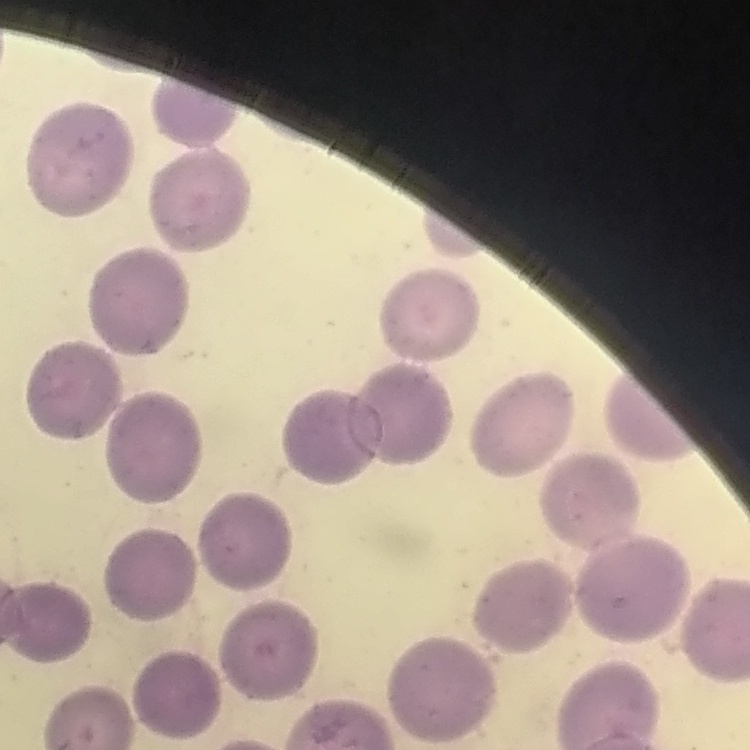
Summary:
  - Red blood cell morphology: no rouleaux formation
  - Stain: Field's or Giemsa
  - Image type: square crop of a larger photomicrograph
  - Preparation: thin blood smear